State the blood parasite species.
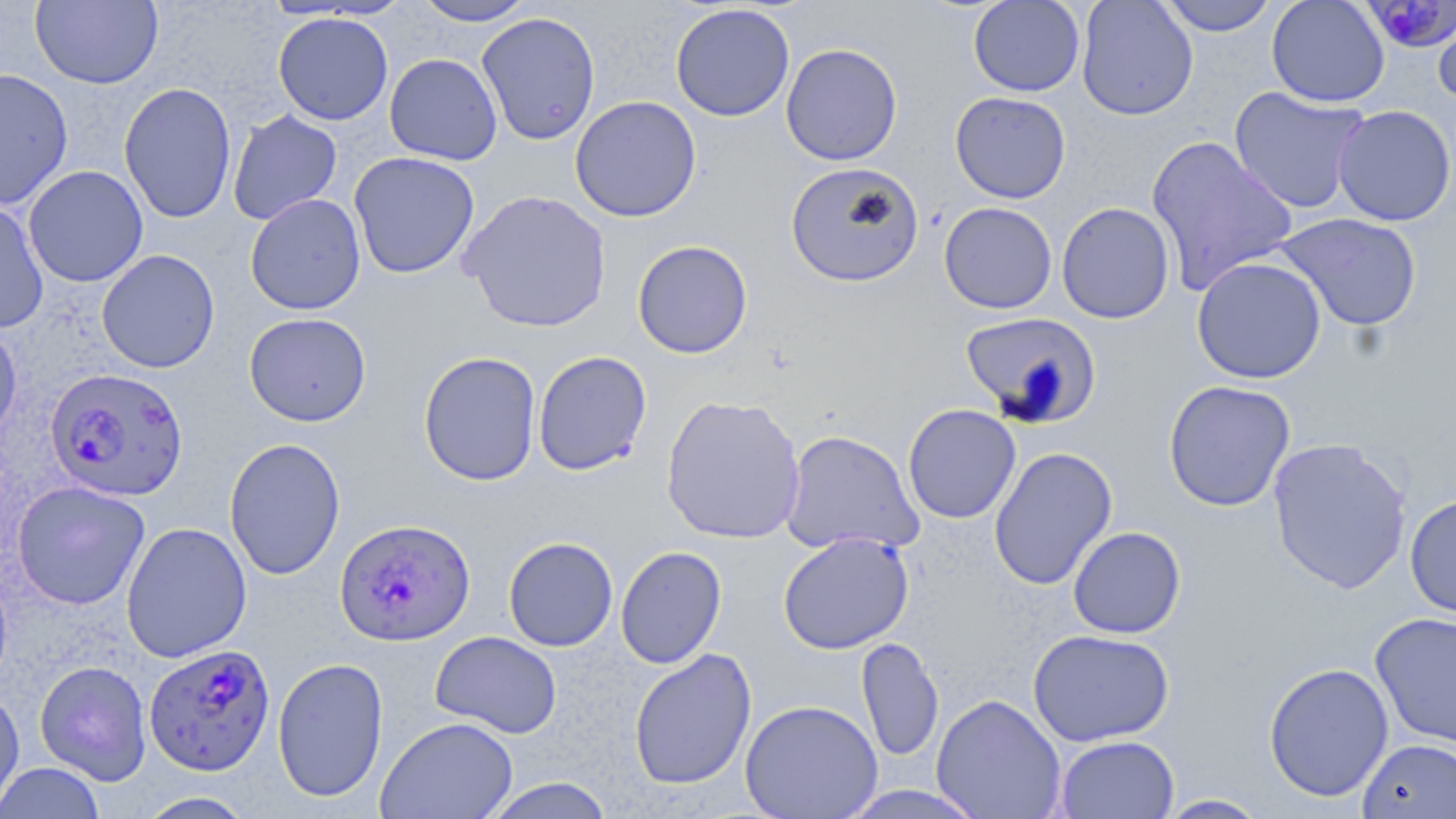

Plasmodium falciparum.

Approximate bounding boxes as [x1, y1, x2, y2] in pixels. Plasmodium falciparum-infected red blood cell locations: [1369, 2, 1455, 57], [44, 367, 188, 502], [334, 518, 475, 646], [144, 643, 276, 776]. Uninfected red blood cell locations: [31, 0, 163, 89], [413, 0, 538, 26], [968, 0, 1085, 97], [1076, 0, 1198, 121], [1157, 0, 1278, 36], [1266, 0, 1390, 108], [670, 4, 796, 122], [1433, 4, 1456, 107], [476, 11, 600, 146], [272, 12, 394, 125], [781, 43, 903, 165], [385, 53, 503, 165], [0, 68, 73, 210], [118, 82, 237, 224], [1229, 85, 1370, 215], [949, 91, 1071, 203], [570, 95, 702, 222], [1332, 105, 1456, 226], [227, 109, 343, 225], [1145, 135, 1298, 295], [349, 151, 480, 279], [785, 161, 924, 288], [23, 165, 149, 287], [458, 189, 612, 334], [245, 193, 366, 315], [0, 200, 49, 334], [939, 201, 1057, 314], [1057, 202, 1175, 324], [1274, 212, 1422, 333], [632, 240, 753, 359], [96, 249, 220, 373], [1191, 256, 1326, 384], [960, 311, 1101, 427], [244, 312, 371, 426], [0, 320, 22, 446], [533, 350, 652, 476], [418, 351, 542, 486], [1163, 380, 1295, 511], [660, 394, 806, 545], [903, 403, 1021, 524], [780, 429, 923, 556], [224, 437, 346, 580], [1267, 437, 1413, 594], [989, 447, 1117, 590], [12, 481, 151, 610], [1404, 493, 1456, 621], [121, 521, 252, 663], [1068, 526, 1186, 638], [778, 532, 914, 654], [503, 537, 618, 651], [615, 546, 727, 669], [1370, 612, 1456, 748], [1027, 629, 1174, 747], [430, 631, 562, 739], [856, 637, 943, 764], [628, 648, 757, 790], [272, 657, 389, 803], [34, 660, 153, 785], [1263, 662, 1394, 803], [0, 686, 25, 818], [931, 694, 1067, 818], [740, 699, 882, 819], [376, 716, 518, 818], [1055, 734, 1179, 819], [1356, 737, 1456, 819], [0, 762, 106, 819], [481, 777, 616, 819], [837, 785, 989, 818], [134, 791, 259, 818], [1155, 794, 1271, 818]. 1000x magnification. Image is 1456×819 pixels. May-Grünwald-Giemsa stain. Thin blood film. One field of a larger specimen. Optical microscopy.